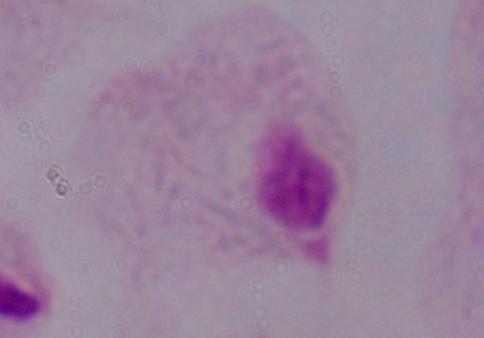
modality = micrograph
magnification = 1000x
identification = trichomonad